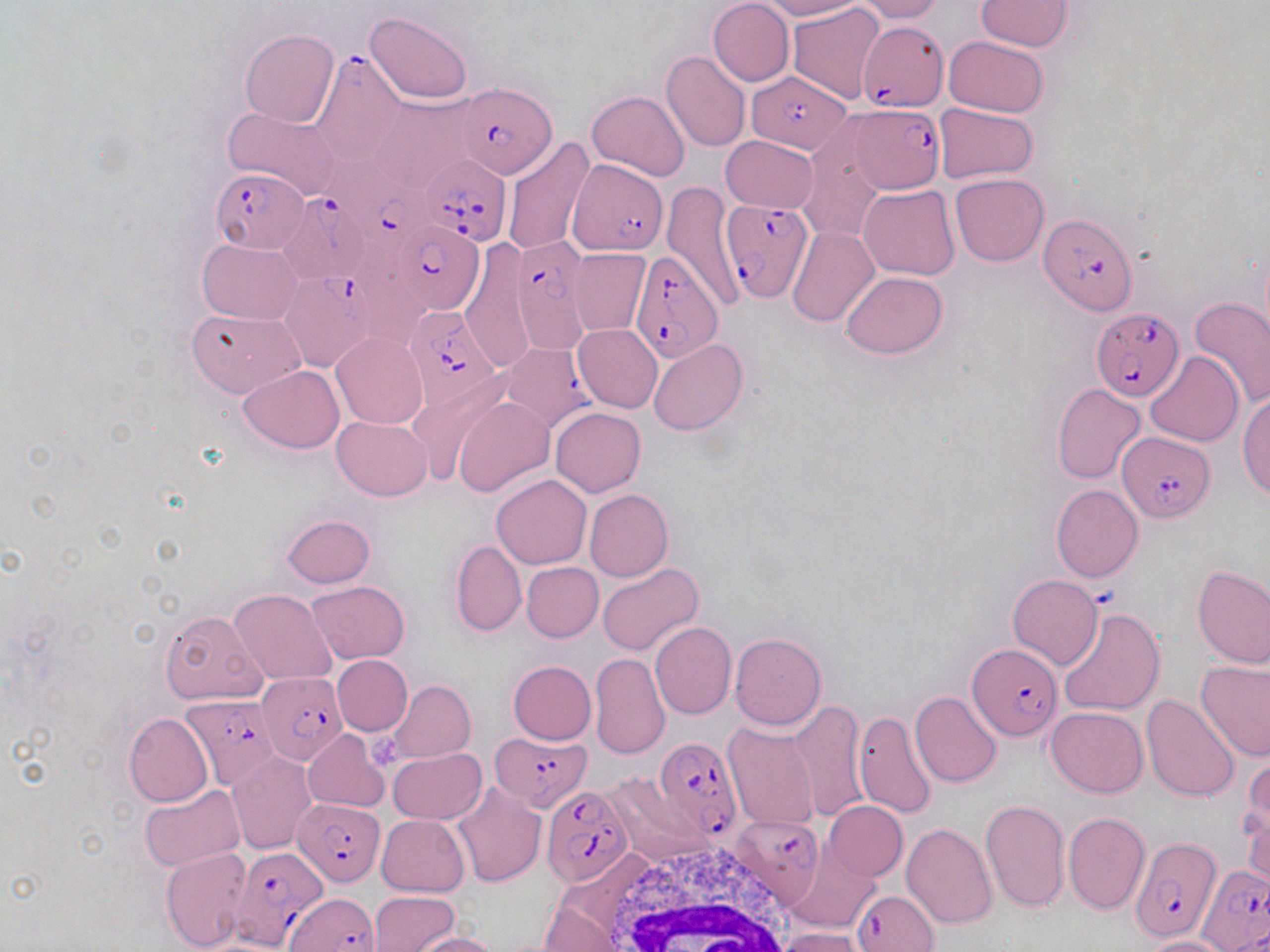

{
  "slide_level_diagnosis": "Plasmodium falciparum",
  "field_of_view": "one of a larger specimen",
  "image_size": "1270×952 pixels",
  "modality": "light microscopy",
  "white_blood_cell_locations": "approximate bounding boxes as [x1, y1, x2, y2] in pixels: [605, 839, 798, 952]",
  "uninfected_red_blood_cell_locations": "approximate bounding boxes as [x1, y1, x2, y2] in pixels: [707, 0, 794, 86], [758, 0, 861, 19], [853, 0, 943, 22], [976, 1, 1073, 50], [788, 3, 885, 103], [365, 11, 474, 104], [240, 28, 338, 128], [944, 36, 1049, 116], [661, 49, 750, 152], [587, 90, 690, 182], [373, 93, 483, 190], [934, 103, 1039, 183], [223, 107, 344, 201], [798, 132, 887, 244], [720, 136, 817, 214], [501, 137, 594, 257], [949, 174, 1049, 266], [662, 180, 746, 311], [858, 185, 960, 281], [787, 226, 879, 327], [199, 239, 302, 323], [458, 243, 536, 374], [569, 248, 649, 337], [841, 271, 948, 358], [1189, 297, 1270, 408], [187, 307, 305, 397], [572, 324, 662, 413], [331, 331, 428, 429], [648, 339, 747, 436], [1147, 351, 1243, 447], [239, 365, 345, 452], [403, 372, 510, 485], [1052, 384, 1146, 483], [1237, 391, 1270, 500], [454, 394, 555, 497], [551, 407, 645, 496], [333, 415, 432, 500], [491, 475, 591, 569], [1050, 485, 1144, 582], [584, 489, 673, 582], [282, 514, 375, 588], [451, 539, 526, 636], [521, 562, 604, 641], [597, 562, 703, 657], [1192, 564, 1269, 669], [1007, 575, 1101, 669], [306, 581, 410, 663], [230, 589, 336, 685], [160, 609, 267, 704], [1056, 609, 1165, 717], [650, 622, 736, 720], [730, 632, 827, 730], [590, 652, 669, 759], [332, 655, 412, 735], [1195, 659, 1270, 762], [508, 661, 596, 745], [388, 679, 475, 763], [910, 690, 1002, 788], [1141, 695, 1240, 802], [790, 701, 867, 822], [1045, 707, 1149, 797], [852, 711, 937, 819], [124, 713, 212, 807], [722, 723, 819, 830], [303, 728, 390, 813], [388, 747, 487, 825], [227, 753, 317, 854], [1241, 753, 1268, 867], [605, 772, 708, 862], [452, 783, 545, 888], [140, 786, 245, 870], [979, 799, 1069, 914], [822, 801, 907, 881], [1243, 809, 1270, 890], [1063, 811, 1150, 915], [376, 813, 470, 896], [901, 823, 998, 929], [161, 849, 253, 952], [787, 849, 878, 933], [368, 892, 458, 952], [540, 904, 623, 950], [775, 928, 865, 952], [410, 931, 500, 952], [1142, 936, 1233, 952]",
  "preparation": "thin blood film",
  "magnification": "1000x",
  "plasmodium_falciparum_infected_red_blood_cell_locations": "approximate bounding boxes as [x1, y1, x2, y2] in pixels: [860, 24, 948, 117], [309, 50, 407, 165], [747, 72, 850, 152], [456, 82, 556, 178], [845, 101, 946, 193], [419, 154, 512, 247], [568, 160, 669, 256], [213, 168, 309, 253], [277, 190, 374, 285], [721, 197, 813, 300], [1036, 212, 1138, 315], [387, 222, 484, 315], [509, 240, 590, 352], [636, 251, 720, 359], [280, 273, 376, 373], [405, 306, 502, 411], [1091, 310, 1185, 401], [499, 342, 593, 433], [1117, 431, 1216, 523], [967, 643, 1060, 739], [259, 672, 347, 763], [179, 696, 280, 787], [492, 729, 594, 812], [654, 737, 742, 841], [540, 787, 634, 888], [292, 795, 385, 886], [731, 816, 824, 907], [1129, 836, 1220, 942], [224, 847, 330, 947], [1198, 867, 1270, 952], [852, 889, 940, 952], [282, 895, 380, 952]",
  "platelet_locations": "approximate bounding boxes as [x1, y1, x2, y2] in pixels: [366, 727, 405, 771]",
  "stain": "May-Grünwald-Giemsa"
}